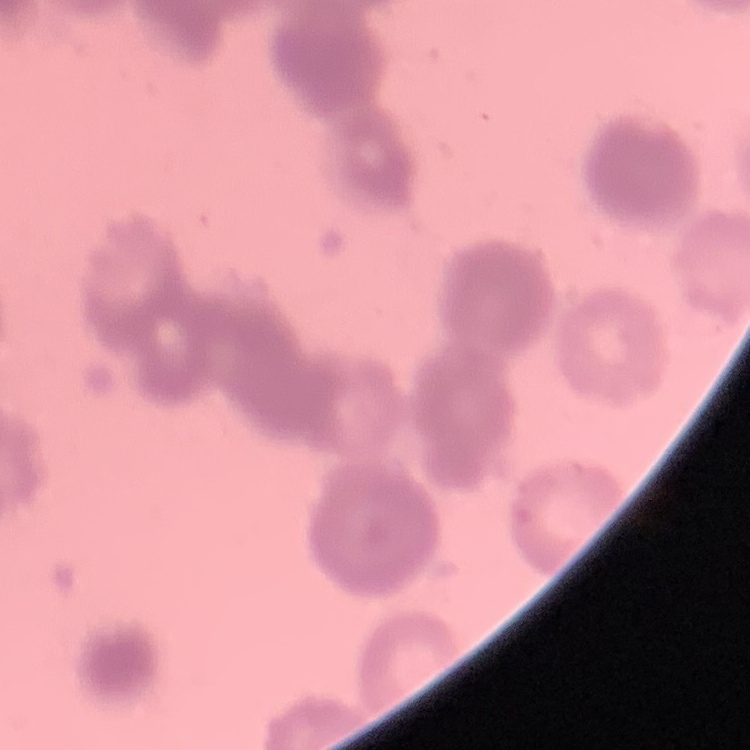
{
  "red_blood_cell_morphology": "rouleaux formation",
  "image_type": "one tile cut from a larger photomicrograph",
  "preparation": "thin peripheral smear",
  "stain": "Field's or Giemsa"
}